Locate every uninfected red blood cell.
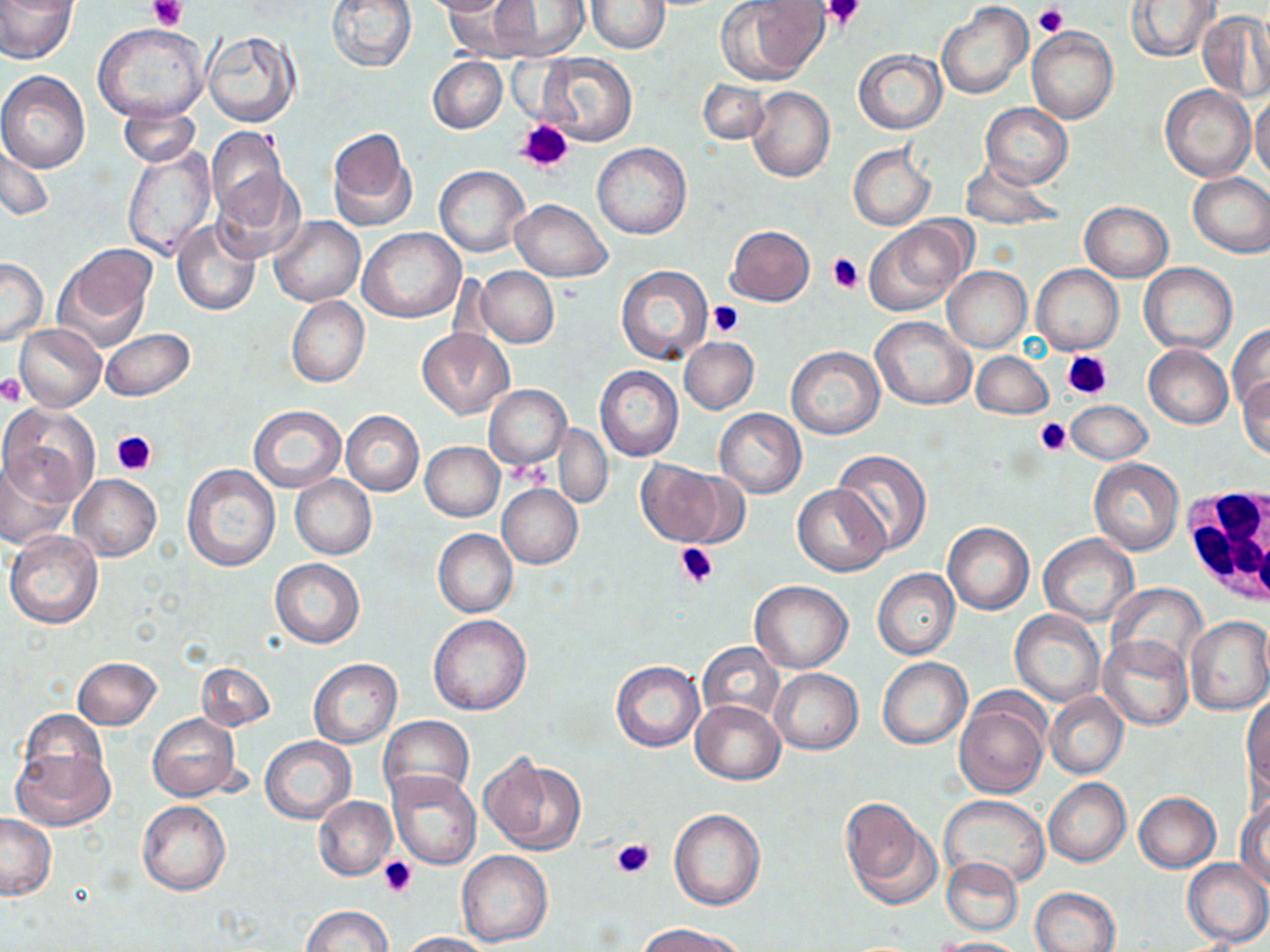
Approximate bounding boxes as (x1,y1)-(x2,y2) corner pairs in pixels.
Uninfected red blood cells: (0,0)-(78,63), (327,0)-(418,72), (423,0)-(510,15), (1126,0)-(1217,63), (492,1)-(588,60), (585,1)-(670,53), (717,1)-(829,85), (937,2)-(1032,99), (1198,10)-(1270,103), (92,25)-(208,124), (1027,26)-(1118,123), (200,29)-(299,127), (853,50)-(946,134), (536,52)-(636,146), (428,56)-(507,133), (0,72)-(90,172), (697,79)-(768,145), (1161,84)-(1255,181), (747,86)-(834,182), (1249,93)-(1270,182), (981,103)-(1072,188), (119,104)-(200,168), (205,127)-(288,223), (326,129)-(415,232), (593,143)-(690,240), (2,144)-(54,220), (849,144)-(935,230), (121,146)-(215,262), (960,158)-(1063,230), (435,166)-(528,257), (212,168)-(307,263), (1188,172)-(1270,258), (511,199)-(612,282), (1079,201)-(1173,281), (269,215)-(364,306), (172,219)-(261,316), (864,221)-(968,316), (726,225)-(815,306), (358,228)-(464,322), (56,245)-(156,350), (1,257)-(48,345), (1140,263)-(1238,353), (616,265)-(712,364), (1031,265)-(1123,354), (943,266)-(1032,352), (476,267)-(559,347), (287,296)-(369,387), (871,316)-(975,410), (15,324)-(105,410), (1228,324)-(1270,417), (101,327)-(194,401), (418,328)-(513,419), (679,338)-(759,414), (1144,344)-(1232,428), (786,346)-(884,439), (972,351)-(1053,420), (595,366)-(683,462), (1237,373)-(1270,458), (484,384)-(571,469), (1066,400)-(1151,464), (1,404)-(99,504), (249,406)-(345,492), (715,408)-(806,498), (341,411)-(424,495), (554,424)-(613,508), (420,441)-(504,520), (832,449)-(932,557), (1088,456)-(1183,554), (1,457)-(75,550), (636,461)-(732,547), (183,464)-(279,571), (71,473)-(160,561), (290,474)-(377,559), (498,483)-(582,568), (793,485)-(890,576), (943,522)-(1034,613), (433,529)-(517,618), (5,530)-(103,629), (1038,534)-(1138,627), (271,559)-(364,646), (873,568)-(959,660), (751,580)-(852,673), (1109,581)-(1206,669), (1010,611)-(1105,707), (428,614)-(531,715), (1184,615)-(1270,716), (1099,636)-(1193,731), (696,643)-(785,727), (878,656)-(970,749), (73,657)-(161,729), (308,657)-(401,749), (195,660)-(275,730), (610,660)-(704,752), (770,668)-(863,754), (1044,691)-(1128,779), (1243,692)-(1269,799), (954,693)-(1050,797), (690,700)-(785,784), (18,710)-(110,795), (146,712)-(242,802), (379,716)-(474,805), (261,737)-(356,824), (12,748)-(114,832), (480,751)-(586,856), (388,771)-(481,870), (1043,777)-(1131,866), (1134,791)-(1221,872), (938,795)-(1050,889), (315,796)-(397,880), (1236,799)-(1270,888), (840,800)-(939,910), (137,801)-(230,896), (670,808)-(765,910), (0,814)-(55,900), (456,851)-(551,947), (941,857)-(1023,937), (1182,857)-(1270,946), (1029,887)-(1120,952), (301,906)-(391,952), (638,922)-(746,952), (400,931)-(495,951), (932,937)-(1024,951).

White blood cell locations: (1185,481)-(1270,610). Platelet locations: (147,0)-(186,31), (819,0)-(867,31), (1034,3)-(1069,36), (515,119)-(574,174), (827,252)-(862,294), (708,300)-(744,338), (1063,349)-(1113,402), (0,376)-(25,406), (1035,418)-(1073,457), (113,429)-(158,476), (675,543)-(718,589), (610,838)-(655,880), (379,858)-(420,899). Slide-level diagnosis: no evidence of blood parasites. One field of a larger specimen. 1000x magnification. Light microscopy. May-Grünwald-Giemsa-stained preparation. Thin blood smear. Image is 1270×952 pixels.